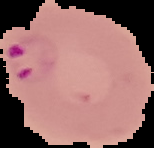
{
  "image_size": "154×148 pixels",
  "result": "malaria parasites detected",
  "image_type": "segmented cell region with the area outside set to black",
  "preparation": "thin blood film"
}